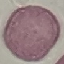
Summary:
  - Result: no malaria parasites detected
  - Image type: automatically extracted cell patch, resized to 64 × 64 pixels
  - Stain: Giemsa
  - Preparation: thin blood film
  - Capture: smartphone through the microscope eyepiece